Report the malaria status of this cell.
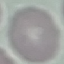

It is uninfected.

capture = smartphone camera at the microscope eyepiece
image type = automatically extracted cell patch, resized to 64 × 64 pixels
preparation = thin blood smear
stain = Giemsa